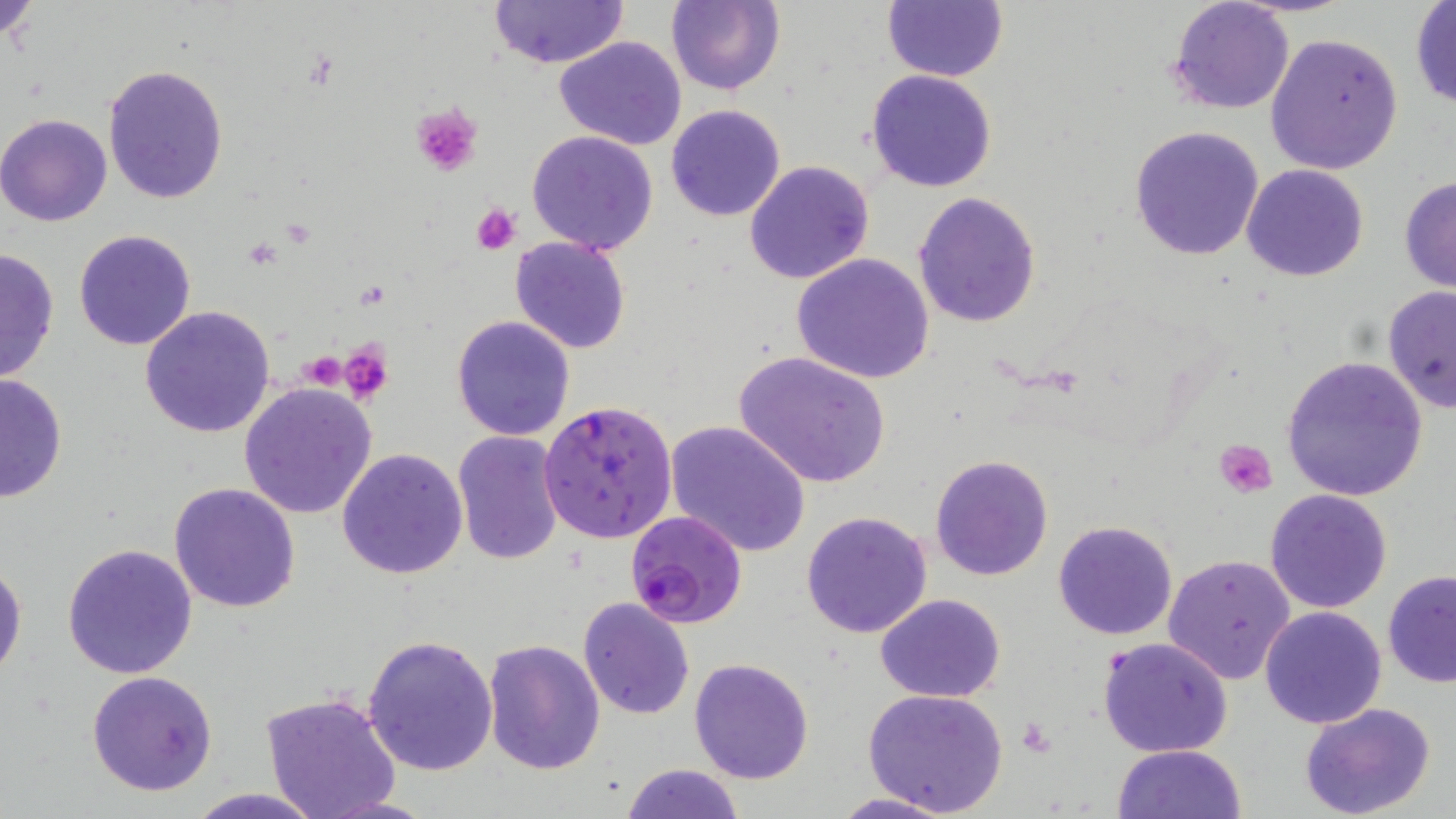

Approximate bounding boxes as [x1, y1, x2, y2] in pixels. Plasmodium falciparum-infected red blood cell locations: [538, 399, 677, 544], [624, 509, 747, 630]. Platelet locations: [407, 102, 484, 176], [473, 202, 520, 254], [336, 339, 391, 405], [301, 351, 347, 394], [1215, 439, 1278, 498], [1019, 716, 1054, 756]. Uninfected red blood cell locations: [0, 0, 45, 49], [487, 0, 628, 69], [665, 0, 786, 95], [881, 0, 1006, 83], [1168, 0, 1295, 115], [1409, 2, 1456, 109], [1265, 33, 1403, 174], [554, 36, 687, 151], [102, 64, 229, 204], [867, 68, 998, 192], [665, 104, 787, 222], [0, 113, 113, 227], [1128, 125, 1268, 262], [526, 130, 660, 257], [744, 160, 875, 285], [1241, 164, 1368, 282], [1399, 176, 1456, 294], [914, 191, 1041, 328], [72, 229, 198, 351], [510, 235, 632, 354], [0, 246, 60, 385], [790, 253, 934, 383], [1382, 285, 1456, 413], [139, 305, 276, 438], [451, 315, 576, 440], [733, 350, 893, 488], [1279, 355, 1429, 502], [0, 372, 67, 503], [238, 382, 378, 521], [664, 420, 811, 558], [452, 430, 565, 565], [337, 447, 469, 580], [930, 453, 1055, 580], [169, 481, 301, 613], [1264, 487, 1395, 613], [801, 511, 933, 639], [1052, 518, 1180, 640], [61, 542, 199, 679], [1163, 553, 1297, 684], [0, 556, 26, 678], [1382, 572, 1456, 689], [875, 594, 1006, 702], [577, 596, 696, 719], [1259, 606, 1388, 730], [360, 635, 500, 776], [1098, 635, 1233, 757], [481, 638, 605, 777], [689, 658, 814, 784], [87, 670, 219, 795], [862, 687, 1008, 815], [259, 692, 402, 819], [1299, 703, 1438, 819], [1113, 745, 1245, 819], [620, 762, 747, 819], [183, 788, 330, 819], [827, 791, 960, 818]. Slide-level diagnosis: Plasmodium falciparum. Optical microscopy. Thin blood smear. Single field of view. 1000x magnification. May-Grünwald-Giemsa stain. Image is 1456×819 pixels.